Locate every Plasmodium falciparum-infected red blood cell.
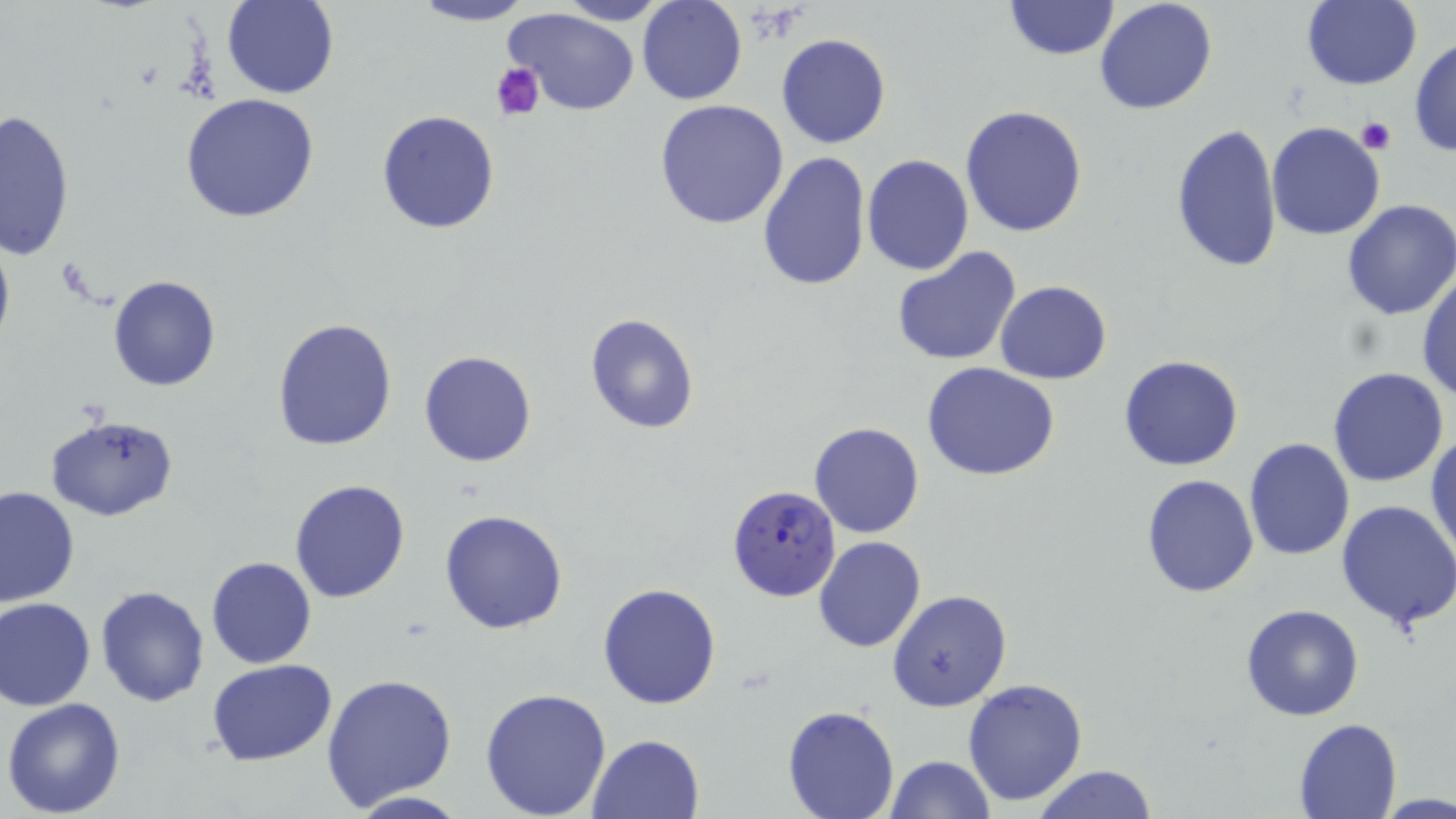

Approximate bounding boxes as named x1/y1/x2/y2 corners in pixels.
Plasmodium falciparum-infected red blood cells: (x1=727, y1=485, x2=840, y2=602).

Summary:
  - Uninfected red blood cell locations: (x1=553, y1=0, x2=675, y2=25), (x1=637, y1=0, x2=746, y2=105), (x1=1094, y1=0, x2=1218, y2=115), (x1=222, y1=1, x2=339, y2=99), (x1=407, y1=1, x2=536, y2=26), (x1=1001, y1=1, x2=1121, y2=61), (x1=1300, y1=1, x2=1422, y2=90), (x1=505, y1=8, x2=641, y2=115), (x1=776, y1=34, x2=891, y2=149), (x1=1409, y1=36, x2=1456, y2=157), (x1=180, y1=94, x2=321, y2=224), (x1=654, y1=98, x2=790, y2=230), (x1=960, y1=105, x2=1088, y2=237), (x1=1, y1=108, x2=75, y2=259), (x1=375, y1=109, x2=500, y2=235), (x1=1266, y1=122, x2=1385, y2=241), (x1=1170, y1=123, x2=1282, y2=272), (x1=757, y1=150, x2=872, y2=291), (x1=861, y1=155, x2=973, y2=275), (x1=1341, y1=201, x2=1456, y2=320), (x1=0, y1=223, x2=16, y2=360), (x1=891, y1=247, x2=1023, y2=365), (x1=1416, y1=270, x2=1456, y2=406), (x1=106, y1=276, x2=221, y2=392), (x1=994, y1=280, x2=1111, y2=384), (x1=584, y1=312, x2=701, y2=436), (x1=273, y1=317, x2=398, y2=450), (x1=419, y1=349, x2=537, y2=466), (x1=1119, y1=354, x2=1245, y2=472), (x1=921, y1=363, x2=1062, y2=481), (x1=1327, y1=366, x2=1450, y2=487), (x1=46, y1=413, x2=177, y2=522), (x1=809, y1=420, x2=924, y2=539), (x1=1427, y1=430, x2=1455, y2=563), (x1=1244, y1=438, x2=1355, y2=559), (x1=1140, y1=473, x2=1259, y2=598), (x1=289, y1=479, x2=412, y2=604), (x1=0, y1=485, x2=79, y2=607), (x1=1335, y1=499, x2=1456, y2=631), (x1=440, y1=508, x2=569, y2=633), (x1=813, y1=536, x2=926, y2=655), (x1=206, y1=557, x2=316, y2=669), (x1=597, y1=582, x2=722, y2=709), (x1=95, y1=585, x2=209, y2=706), (x1=888, y1=590, x2=1011, y2=712), (x1=1, y1=597, x2=97, y2=711), (x1=1240, y1=603, x2=1364, y2=721), (x1=208, y1=659, x2=337, y2=765), (x1=321, y1=674, x2=457, y2=810), (x1=962, y1=679, x2=1088, y2=807), (x1=479, y1=685, x2=612, y2=817), (x1=3, y1=698, x2=127, y2=818), (x1=783, y1=706, x2=899, y2=819), (x1=1294, y1=717, x2=1400, y2=819), (x1=589, y1=734, x2=706, y2=819), (x1=885, y1=755, x2=996, y2=818), (x1=1031, y1=765, x2=1159, y2=819), (x1=344, y1=791, x2=473, y2=819)
  - Platelet locations: (x1=489, y1=60, x2=546, y2=121), (x1=1358, y1=116, x2=1396, y2=153)
  - Slide-level diagnosis: Plasmodium falciparum
  - Magnification: 1000x
  - Field of view: single
  - Modality: optical microscopy
  - Preparation: thin blood smear
  - Image size: 1456×819 pixels
  - Stain: May-Grünwald-Giemsa